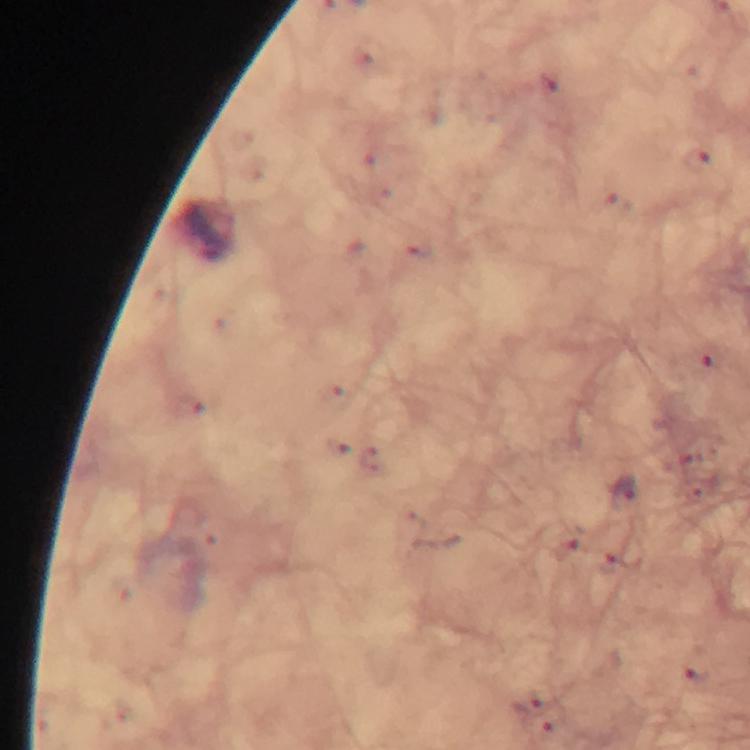
Approximate centers as {x, y} in pixels.
Summary:
  - Malaria parasite locations: {695, 159}, {622, 490}
  - Stain: Giemsa
  - Image size: 750×750 pixels
  - Cropped from: a single field of view
  - Preparation: thick blood smear
  - Magnification: 100x
  - Context: from a diagnostic examination for malaria
  - Immersion oil: applied
  - Capture: smartphone camera through the microscope